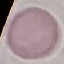
Summary:
  - Result: no malaria parasites seen
  - Capture: smartphone through the microscope eyepiece
  - Preparation: thin blood smear
  - Image type: automatically extracted cell patch, resized to 64 × 64 pixels
  - Stain: Giemsa